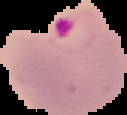

Summary:
  - Image type: segmented cell region with the area outside set to black
  - Preparation: thin blood film
  - Result: malaria parasites detected
  - Image size: 127×115 pixels